Outline each blood parasite and name the species.
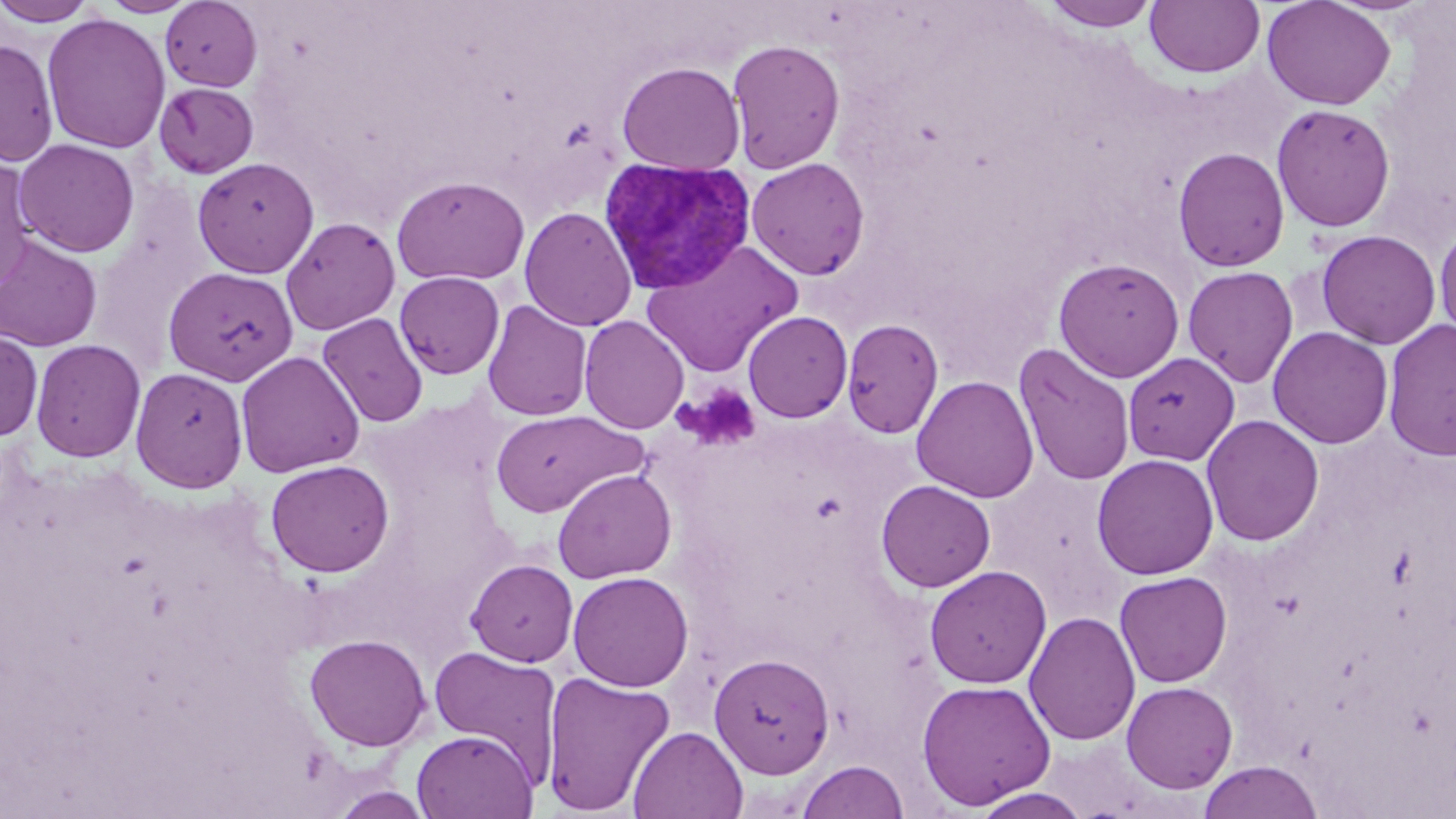
Approximate bounding boxes as [x1, y1, x2, y2] in pixels.
Plasmodium vivax-infected red blood cells: [598, 158, 755, 295].
No Plasmodium falciparum, Plasmodium ovale, Plasmodium malariae, Babesia divergens, or Trypanosoma brucei observed.

slide-level diagnosis = Plasmodium vivax
stain = May-Grünwald-Giemsa
magnification = 1000x
modality = optical microscopy
preparation = thin blood smear
field of view = single
platelet locations = approximate bounding boxes as [x1, y1, x2, y2] in pixels: [682, 384, 762, 451]
image size = 1456×819 pixels
uninfected red blood cell locations = approximate bounding boxes as [x1, y1, x2, y2] in pixels: [0, 0, 100, 26], [99, 0, 198, 17], [1261, 0, 1396, 111], [160, 1, 264, 92], [1040, 1, 1163, 32], [1145, 1, 1266, 79], [41, 14, 172, 154], [0, 38, 59, 166], [726, 38, 846, 174], [617, 61, 745, 174], [154, 82, 259, 179], [1271, 103, 1396, 232], [14, 139, 140, 256], [1172, 147, 1290, 272], [192, 157, 319, 278], [746, 157, 870, 280], [0, 159, 38, 292], [391, 175, 530, 286], [519, 206, 637, 331], [280, 216, 401, 335], [1434, 221, 1456, 346], [1316, 229, 1441, 350], [0, 235, 103, 352], [641, 241, 803, 378], [1053, 257, 1185, 382], [1182, 265, 1298, 388], [162, 267, 299, 386], [394, 271, 506, 379], [482, 300, 593, 421], [742, 310, 853, 423], [317, 312, 429, 428], [579, 315, 689, 435], [841, 318, 945, 438], [1383, 319, 1456, 462], [1267, 326, 1393, 449], [0, 330, 43, 442], [30, 338, 146, 462], [1013, 342, 1136, 487], [235, 350, 365, 477], [1123, 353, 1240, 464], [130, 367, 248, 493], [912, 375, 1039, 503], [489, 408, 646, 518], [1201, 414, 1324, 547], [1092, 454, 1219, 580], [265, 459, 394, 577], [552, 468, 677, 583], [876, 479, 995, 592], [465, 558, 578, 666], [924, 565, 1052, 689], [568, 570, 694, 692], [1114, 571, 1232, 687], [1024, 611, 1140, 746], [304, 633, 431, 752], [427, 644, 563, 780], [708, 652, 835, 778], [540, 670, 676, 816], [916, 678, 1056, 810], [1121, 681, 1238, 793], [628, 726, 748, 818], [412, 731, 537, 818], [796, 760, 909, 819], [1197, 761, 1325, 819], [328, 786, 436, 818], [967, 787, 1095, 818]